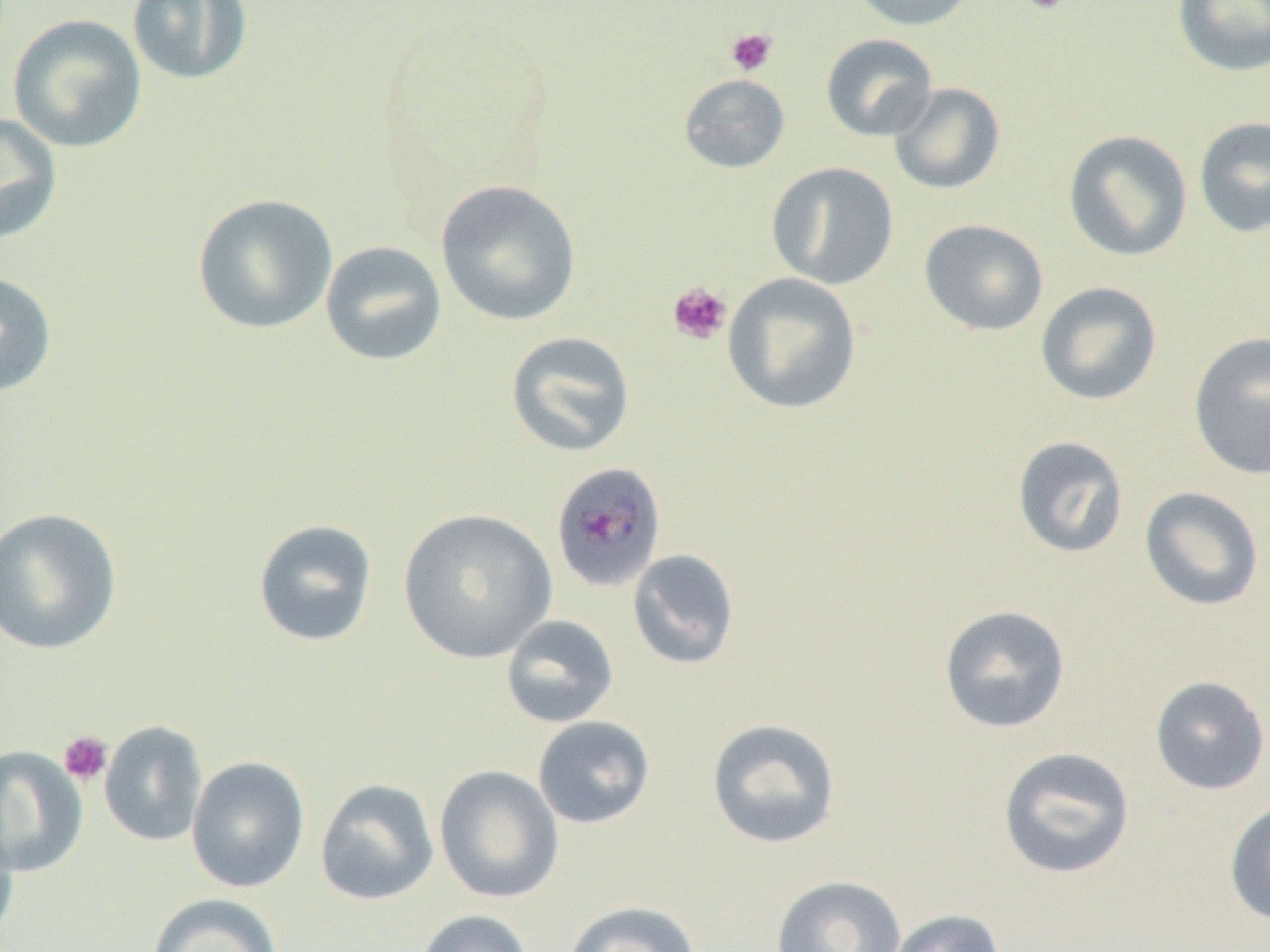

Approximate bounding boxes as named x1/y1/x2/y2 corners in pixels. Plasmodium malariae-infected red blood cell locations: (x1=550, y1=462, x2=667, y2=592). Uninfected red blood cell locations: (x1=127, y1=0, x2=253, y2=86), (x1=844, y1=0, x2=980, y2=32), (x1=1172, y1=0, x2=1270, y2=77), (x1=7, y1=14, x2=147, y2=154), (x1=820, y1=33, x2=938, y2=141), (x1=678, y1=73, x2=791, y2=174), (x1=888, y1=82, x2=1006, y2=195), (x1=0, y1=112, x2=62, y2=244), (x1=1193, y1=115, x2=1270, y2=239), (x1=1063, y1=129, x2=1193, y2=262), (x1=766, y1=161, x2=899, y2=290), (x1=435, y1=179, x2=582, y2=326), (x1=192, y1=194, x2=339, y2=335), (x1=918, y1=218, x2=1049, y2=337), (x1=320, y1=240, x2=447, y2=366), (x1=0, y1=271, x2=58, y2=398), (x1=723, y1=273, x2=862, y2=415), (x1=1035, y1=282, x2=1163, y2=405), (x1=506, y1=331, x2=636, y2=458), (x1=1188, y1=331, x2=1270, y2=482), (x1=1011, y1=434, x2=1130, y2=559), (x1=1139, y1=486, x2=1265, y2=612), (x1=0, y1=507, x2=123, y2=655), (x1=397, y1=508, x2=557, y2=664), (x1=252, y1=518, x2=378, y2=648), (x1=627, y1=549, x2=740, y2=670), (x1=938, y1=604, x2=1071, y2=734), (x1=500, y1=614, x2=620, y2=729), (x1=1149, y1=675, x2=1270, y2=795), (x1=532, y1=715, x2=656, y2=829), (x1=706, y1=718, x2=842, y2=850), (x1=99, y1=721, x2=209, y2=846), (x1=0, y1=745, x2=88, y2=877), (x1=997, y1=746, x2=1136, y2=879), (x1=186, y1=756, x2=310, y2=893), (x1=433, y1=765, x2=565, y2=904), (x1=314, y1=779, x2=440, y2=906), (x1=1224, y1=800, x2=1270, y2=927), (x1=0, y1=810, x2=20, y2=947), (x1=770, y1=874, x2=908, y2=952), (x1=145, y1=893, x2=284, y2=952), (x1=563, y1=901, x2=702, y2=952), (x1=885, y1=908, x2=1006, y2=952), (x1=414, y1=909, x2=536, y2=952). Platelet locations: (x1=1019, y1=0, x2=1070, y2=15), (x1=725, y1=27, x2=778, y2=77), (x1=666, y1=281, x2=732, y2=345), (x1=58, y1=731, x2=113, y2=787). Slide-level diagnosis: Plasmodium malariae. Single field of view. Optical microscopy. Image is 1270×952 pixels. Captured at 1000x magnification. Thin blood smear.